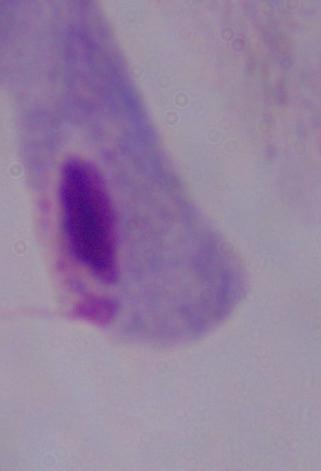
Summary:
  - Magnification: 1000x
  - Modality: micrograph
  - Identification: trichomonad